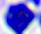
modality = photomicrograph
magnification = 400x
identification = leukocyte